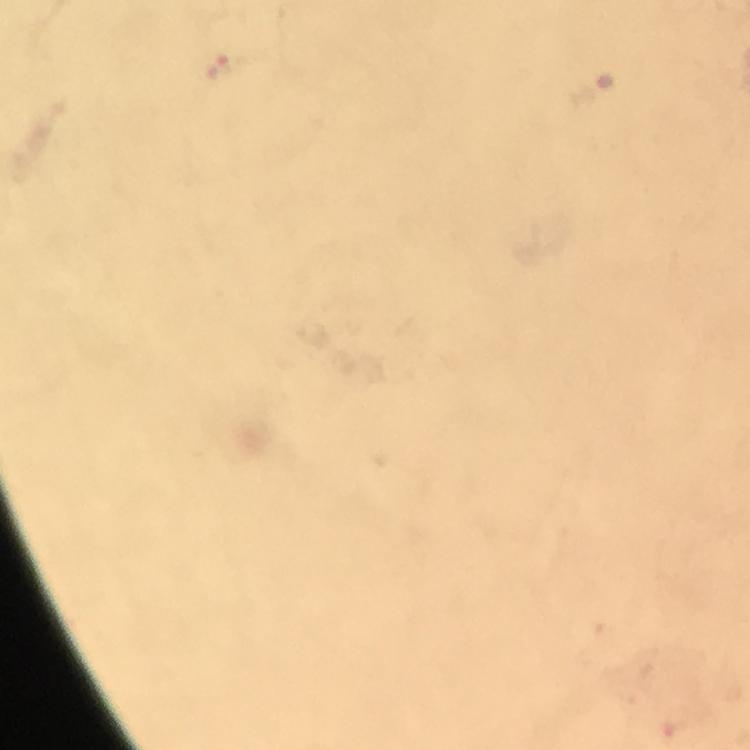
capture = smartphone mounted on the microscope
context = from a diagnostic examination for malaria
image size = 750×750 pixels
immersion oil = used
preparation = thick blood smear
stain = Giemsa
magnification = 100x
cropped from = one field of view
Plasmodium parasite locations = approximate centers as [x, y] in pixels: [223, 65]